State which parasite is depicted.
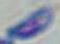
Toxoplasma gondii.

Summary:
  - Modality: photomicrograph
  - Magnification: 1000x